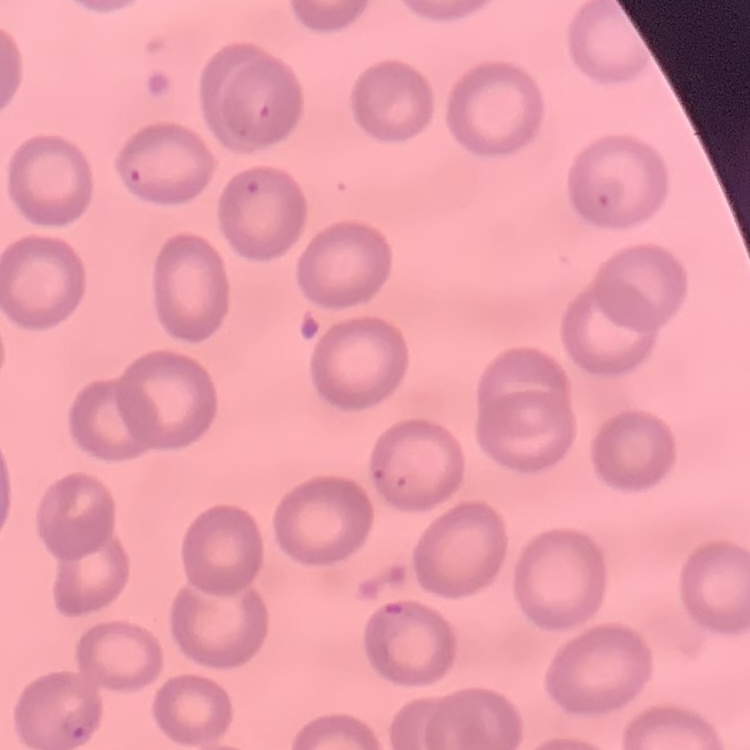
The red blood cells exhibit no rouleaux formation. Thin peripheral smear. One tile cut from a larger photomicrograph. Stained with either Field's or Giemsa.